Describe the morphology of the erythrocytes.
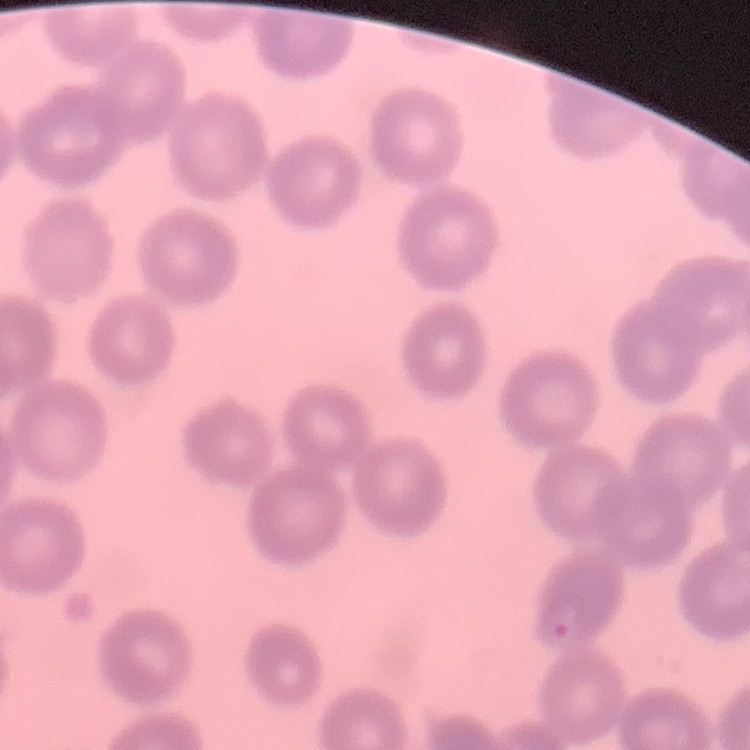
No rouleaux formation.

image type = square crop of a larger photomicrograph
stain = Field's or Giemsa
preparation = thin blood smear